Report the malaria status of this cell.
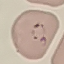

Parasitized.

Automatically extracted cell patch, resized to 64 × 64 pixels. Photographed with a smartphone camera at the microscope eyepiece. Giemsa-stained preparation. Thin blood smear.